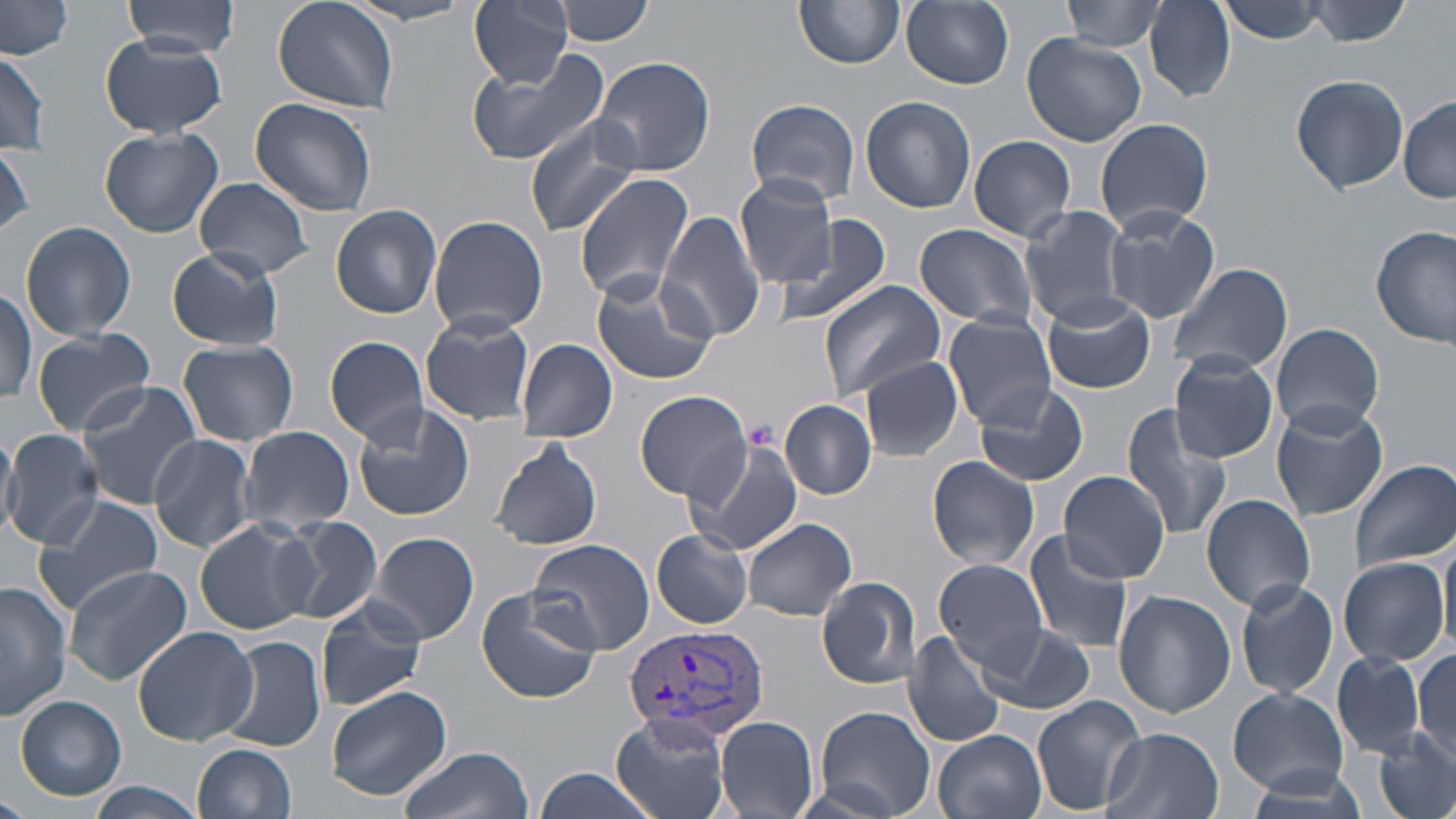
Plasmodium vivax-infected red blood cell locations = approximate bounding boxes as named x1/y1/x2/y2 corners in pixels: (x1=621, y1=625, x2=770, y2=742)
slide-level diagnosis = Plasmodium vivax
magnification = 1000x
image size = 1456×819 pixels
platelet locations = approximate bounding boxes as named x1/y1/x2/y2 corners in pixels: (x1=744, y1=419, x2=777, y2=448)
stain = May-Grünwald-Giemsa
modality = light microscopy
preparation = thin blood film
uninfected red blood cell locations = approximate bounding boxes as named x1/y1/x2/y2 corners in pixels: (x1=123, y1=0, x2=240, y2=57), (x1=273, y1=0, x2=397, y2=114), (x1=468, y1=0, x2=574, y2=88), (x1=556, y1=0, x2=654, y2=45), (x1=796, y1=0, x2=904, y2=71), (x1=1063, y1=0, x2=1164, y2=52), (x1=1218, y1=0, x2=1331, y2=44), (x1=1305, y1=0, x2=1415, y2=46), (x1=0, y1=1, x2=74, y2=61), (x1=900, y1=1, x2=1014, y2=90), (x1=1146, y1=1, x2=1235, y2=102), (x1=345, y1=2, x2=473, y2=26), (x1=1023, y1=32, x2=1146, y2=146), (x1=101, y1=35, x2=225, y2=137), (x1=0, y1=44, x2=53, y2=158), (x1=463, y1=44, x2=613, y2=166), (x1=0, y1=48, x2=51, y2=155), (x1=590, y1=56, x2=714, y2=177), (x1=1291, y1=73, x2=1411, y2=195), (x1=860, y1=95, x2=976, y2=212), (x1=1400, y1=96, x2=1456, y2=203), (x1=250, y1=97, x2=378, y2=216), (x1=745, y1=99, x2=860, y2=207), (x1=524, y1=115, x2=647, y2=236), (x1=1095, y1=117, x2=1214, y2=236), (x1=99, y1=127, x2=222, y2=238), (x1=968, y1=135, x2=1077, y2=241), (x1=0, y1=144, x2=33, y2=237), (x1=574, y1=173, x2=696, y2=302), (x1=735, y1=175, x2=840, y2=286), (x1=194, y1=179, x2=317, y2=279), (x1=1019, y1=205, x2=1132, y2=327), (x1=331, y1=206, x2=443, y2=319), (x1=1101, y1=207, x2=1222, y2=324), (x1=656, y1=210, x2=767, y2=342), (x1=775, y1=214, x2=896, y2=327), (x1=428, y1=215, x2=548, y2=336), (x1=21, y1=222, x2=136, y2=342), (x1=915, y1=223, x2=1038, y2=328), (x1=1372, y1=224, x2=1455, y2=352), (x1=165, y1=246, x2=285, y2=352), (x1=1168, y1=260, x2=1293, y2=379), (x1=589, y1=271, x2=720, y2=386), (x1=818, y1=280, x2=946, y2=406), (x1=0, y1=288, x2=37, y2=408), (x1=1040, y1=294, x2=1157, y2=394), (x1=419, y1=312, x2=536, y2=426), (x1=943, y1=312, x2=1058, y2=429), (x1=1270, y1=323, x2=1385, y2=439), (x1=32, y1=328, x2=158, y2=437), (x1=325, y1=334, x2=431, y2=445), (x1=517, y1=339, x2=617, y2=443), (x1=178, y1=340, x2=298, y2=446), (x1=1169, y1=353, x2=1280, y2=464), (x1=861, y1=359, x2=964, y2=462), (x1=73, y1=380, x2=205, y2=509), (x1=972, y1=380, x2=1091, y2=488), (x1=633, y1=390, x2=751, y2=502), (x1=781, y1=400, x2=876, y2=500), (x1=352, y1=402, x2=477, y2=522), (x1=1271, y1=402, x2=1388, y2=521), (x1=1118, y1=404, x2=1234, y2=543), (x1=0, y1=425, x2=18, y2=538), (x1=237, y1=426, x2=354, y2=535), (x1=4, y1=430, x2=103, y2=547), (x1=147, y1=434, x2=256, y2=553), (x1=490, y1=437, x2=604, y2=551), (x1=685, y1=437, x2=801, y2=556), (x1=926, y1=455, x2=1039, y2=570), (x1=1350, y1=461, x2=1456, y2=571), (x1=1060, y1=470, x2=1171, y2=582), (x1=32, y1=493, x2=166, y2=615), (x1=1200, y1=495, x2=1316, y2=610), (x1=274, y1=516, x2=384, y2=625), (x1=742, y1=516, x2=858, y2=621), (x1=195, y1=517, x2=319, y2=635), (x1=1024, y1=530, x2=1134, y2=652), (x1=367, y1=531, x2=479, y2=646), (x1=652, y1=531, x2=753, y2=628), (x1=1439, y1=535, x2=1456, y2=657), (x1=526, y1=538, x2=655, y2=655), (x1=1338, y1=555, x2=1451, y2=667), (x1=933, y1=557, x2=1051, y2=674), (x1=61, y1=565, x2=192, y2=686), (x1=817, y1=575, x2=922, y2=690), (x1=1235, y1=577, x2=1339, y2=700), (x1=0, y1=581, x2=71, y2=720), (x1=475, y1=584, x2=601, y2=704), (x1=1113, y1=589, x2=1235, y2=718), (x1=315, y1=599, x2=429, y2=713), (x1=979, y1=624, x2=1097, y2=716), (x1=131, y1=625, x2=258, y2=748), (x1=905, y1=631, x2=1008, y2=751), (x1=218, y1=637, x2=326, y2=754), (x1=1413, y1=650, x2=1456, y2=760), (x1=1333, y1=652, x2=1425, y2=757), (x1=326, y1=685, x2=453, y2=802), (x1=1228, y1=688, x2=1349, y2=798), (x1=1030, y1=693, x2=1147, y2=815), (x1=14, y1=695, x2=126, y2=801), (x1=811, y1=705, x2=935, y2=819), (x1=610, y1=713, x2=732, y2=819), (x1=716, y1=716, x2=819, y2=819), (x1=1101, y1=727, x2=1224, y2=819), (x1=933, y1=730, x2=1045, y2=819), (x1=1373, y1=730, x2=1456, y2=819), (x1=193, y1=743, x2=298, y2=819), (x1=399, y1=745, x2=532, y2=819), (x1=529, y1=769, x2=660, y2=819), (x1=84, y1=780, x2=207, y2=819), (x1=0, y1=789, x2=27, y2=819)
field of view = one of a larger specimen